Identify the parasite.
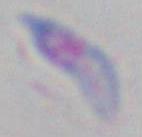

This is Toxoplasma gondii.

Summary:
  - Magnification: 1000x
  - Modality: micrograph